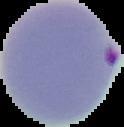 Cell region segmented out of the field of view; the surrounding area is masked to black. From a thin blood smear. Image is 124×127 pixels. Malaria status: parasitized.